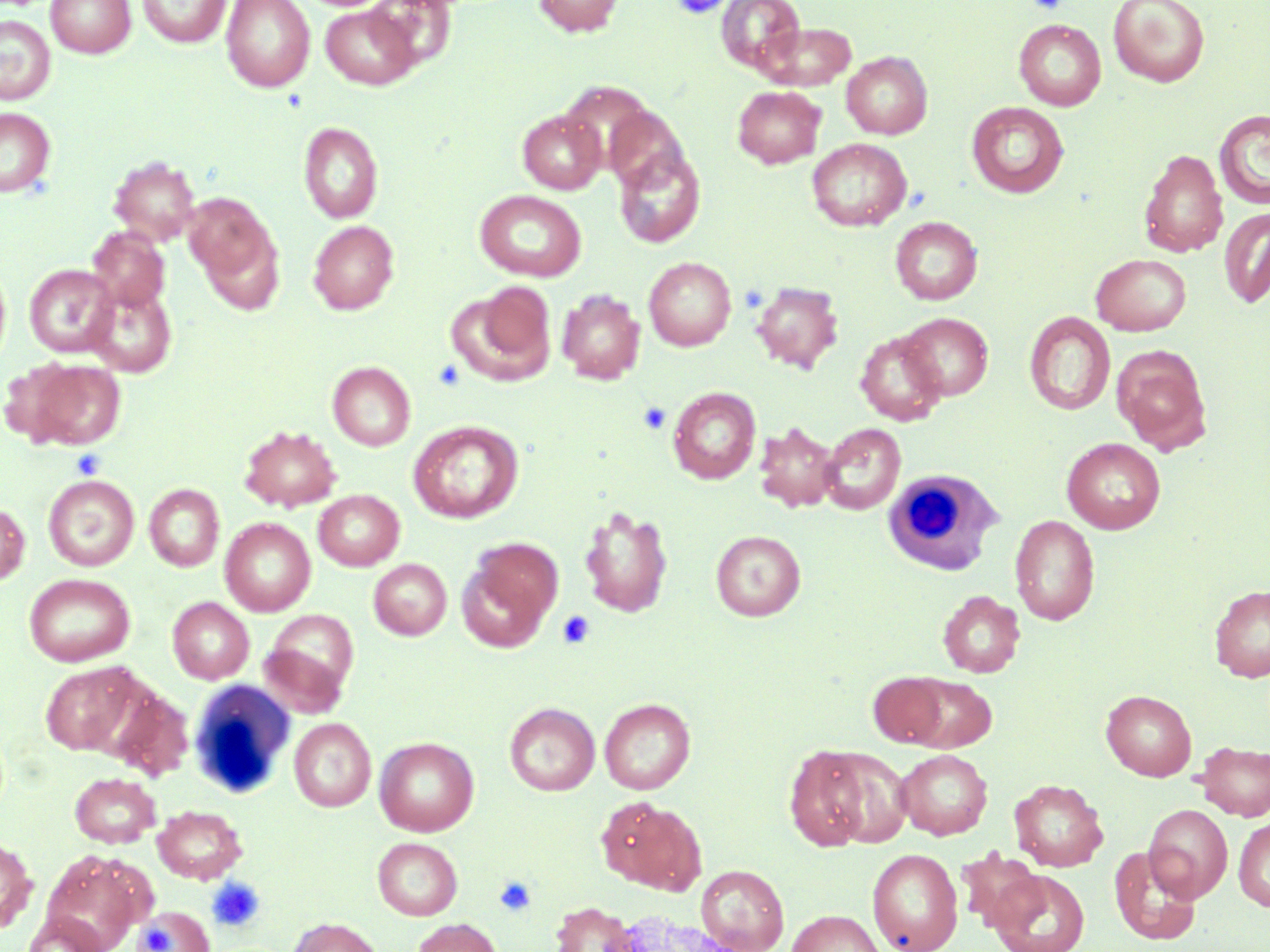

slide_level_diagnosis: negative for blood parasites
platelet_locations: 'approximate bounding boxes as (x1,y1)-(x2,y2) corner pairs in pixels: (671,0)-(730,20), (1026,0)-(1068,13), (739,284)-(768,312), (433,360)-(466,391), (638,401)-(672,435), (70,448)-(106,480), (557,611)-(594,649), (493,876)-(536,917), (206,877)-(266,932), (136,912)-(189,952)'
field_of_view: one of a larger specimen
image_size: 1270×952 pixels
modality: optical microscopy
uninfected_red_blood_cell_locations: 'approximate bounding boxes as (x1,y1)-(x2,y2) corner pairs in pixels: (46,0)-(135,57), (137,0)-(231,48), (221,0)-(315,91), (365,0)-(457,70), (532,0)-(625,37), (716,0)-(804,74), (1108,0)-(1210,87), (320,5)-(420,89), (0,14)-(56,105), (1014,19)-(1106,111), (754,21)-(857,90), (842,51)-(932,139), (733,85)-(826,168), (966,101)-(1069,198), (604,106)-(689,194), (0,107)-(55,197), (517,109)-(606,194), (1215,109)-(1270,209), (298,121)-(383,223), (807,138)-(912,231), (613,149)-(706,248), (1139,149)-(1228,258), (109,156)-(201,245), (475,190)-(587,281), (183,193)-(275,282), (1219,207)-(1270,309), (890,216)-(982,305), (308,220)-(399,314), (199,224)-(286,314), (86,226)-(170,312), (1090,253)-(1191,336), (644,256)-(736,351), (24,264)-(119,357), (754,281)-(844,373), (83,282)-(177,377), (447,285)-(557,387), (557,289)-(645,384), (1024,311)-(1116,416), (899,313)-(993,400), (856,330)-(946,426), (1113,345)-(1210,452), (25,359)-(126,450), (328,361)-(416,451), (668,386)-(761,484), (408,420)-(524,524), (754,423)-(840,512), (819,423)-(906,514), (240,424)-(342,512), (1062,437)-(1166,534), (43,474)-(139,571), (144,483)-(224,571), (313,490)-(405,571), (0,502)-(30,586), (578,504)-(673,619), (1010,514)-(1100,625), (220,517)-(316,616), (711,530)-(805,621), (473,538)-(562,623), (369,558)-(452,640), (456,558)-(553,653), (24,573)-(135,667), (1209,584)-(1270,682), (938,590)-(1025,677), (167,597)-(254,684), (261,610)-(359,710), (39,662)-(143,755), (868,673)-(950,748), (901,673)-(997,752), (102,685)-(194,781), (1101,689)-(1197,781), (599,698)-(695,794), (505,702)-(600,796), (289,718)-(376,811), (375,737)-(479,836), (1196,741)-(1270,821), (784,746)-(876,851), (895,749)-(992,839), (69,772)-(161,847), (1009,779)-(1108,871), (599,797)-(706,894), (1144,803)-(1233,902), (152,804)-(247,884), (1233,816)-(1270,912), (0,837)-(36,934), (373,837)-(462,920), (1109,845)-(1201,945), (867,848)-(963,952), (958,848)-(1044,932), (41,851)-(145,952), (696,864)-(789,952), (989,869)-(1090,952), (552,902)-(639,952), (132,906)-(213,952), (602,907)-(748,952), (787,909)-(887,952), (23,912)-(109,952), (287,917)-(384,952), (411,918)-(502,952)'
preparation: thin blood smear
stain: May-Grünwald-Giemsa
white_blood_cell_locations: 'approximate bounding boxes as (x1,y1)-(x2,y2) corner pairs in pixels: (882,469)-(1003,576), (187,680)-(295,799)'
magnification: 1000x